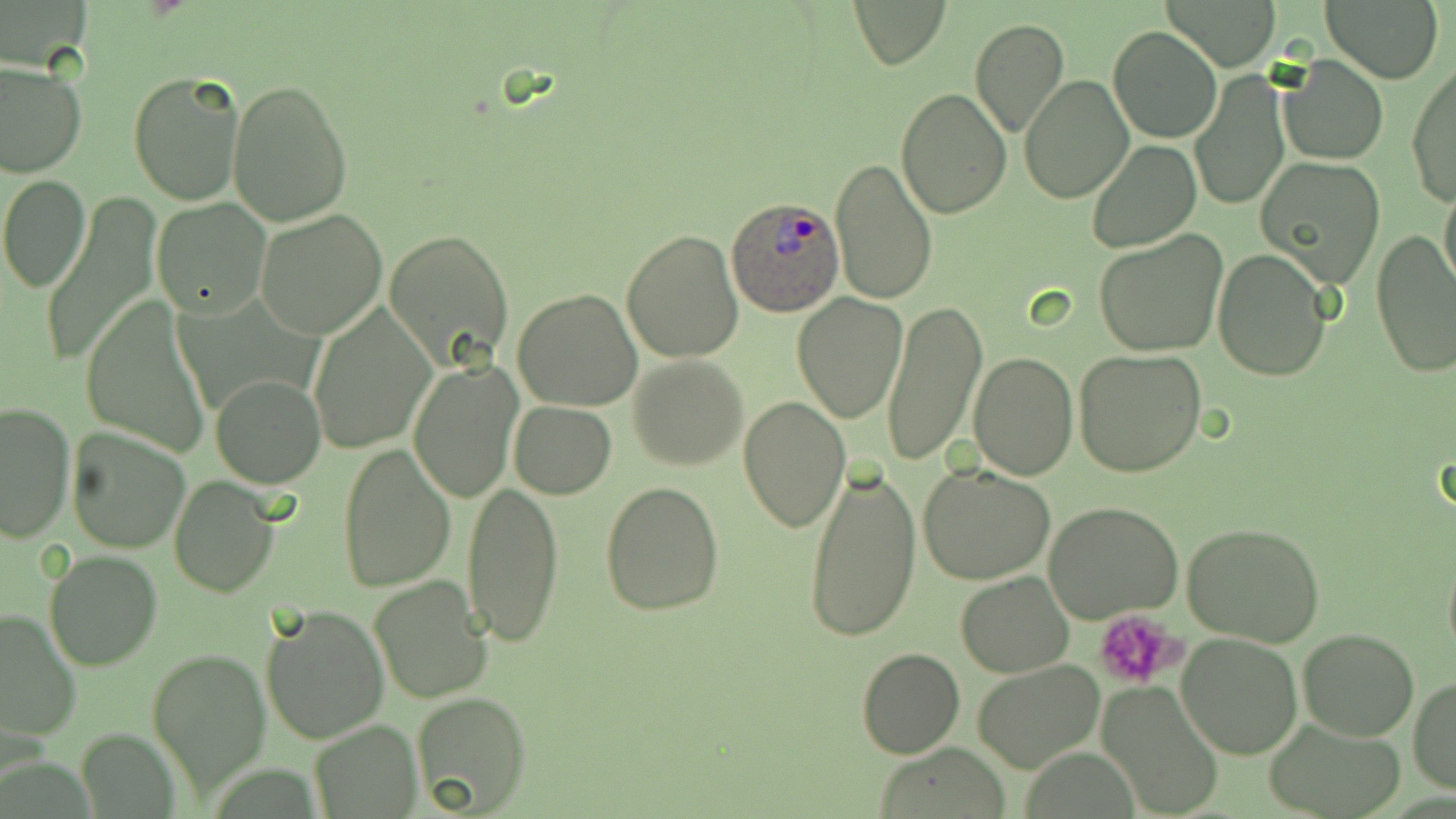

slide_level_diagnosis: Plasmodium ovale
field_of_view: one of a larger specimen
stain: May-Grünwald-Giemsa
uninfected_red_blood_cell_locations: 'approximate bounding boxes as [x1, y1, x2, y2] in pixels: [850, 0, 949, 69], [1165, 0, 1283, 69], [1320, 0, 1445, 84], [969, 18, 1069, 138], [1106, 25, 1222, 144], [1279, 54, 1388, 165], [1406, 60, 1456, 206], [0, 63, 86, 179], [128, 69, 246, 206], [1190, 70, 1290, 211], [1019, 75, 1133, 203], [227, 79, 353, 226], [896, 86, 1012, 218], [1086, 139, 1200, 252], [828, 158, 939, 306], [1257, 158, 1386, 286], [1, 174, 91, 291], [1439, 181, 1456, 297], [40, 193, 159, 371], [150, 197, 271, 318], [255, 209, 388, 339], [622, 228, 745, 363], [388, 229, 513, 365], [1093, 230, 1227, 356], [1370, 231, 1455, 377], [1212, 250, 1331, 381], [511, 288, 643, 412], [791, 293, 908, 426], [882, 298, 986, 467], [82, 299, 211, 456], [306, 305, 435, 454], [1074, 349, 1208, 480], [969, 352, 1078, 480], [627, 355, 748, 472], [407, 358, 524, 503], [210, 375, 325, 488], [738, 394, 850, 533], [0, 400, 77, 542], [509, 401, 616, 498], [66, 425, 194, 553], [336, 442, 457, 593], [804, 462, 920, 645], [919, 463, 1055, 585], [168, 473, 279, 595], [462, 481, 565, 648], [601, 482, 724, 614], [1044, 501, 1183, 624], [1183, 523, 1324, 646], [43, 550, 162, 672], [1442, 551, 1456, 667], [954, 571, 1075, 677], [368, 577, 491, 703], [258, 603, 389, 744], [0, 608, 82, 742], [1297, 629, 1420, 741], [1176, 633, 1303, 759], [146, 646, 270, 793], [856, 647, 965, 760], [973, 660, 1106, 772], [1408, 676, 1456, 796], [1095, 680, 1226, 818], [407, 689, 533, 818], [308, 718, 422, 817], [1264, 719, 1403, 818], [877, 745, 1008, 816]'
platelet_locations: 'approximate bounding boxes as [x1, y1, x2, y2] in pixels: [1092, 610, 1184, 692]'
magnification: 1000x
plasmodium_ovale_infected_red_blood_cell_locations: 'approximate bounding boxes as [x1, y1, x2, y2] in pixels: [727, 195, 844, 316]'
modality: light microscopy
image_size: 1456×819 pixels
preparation: thin blood film